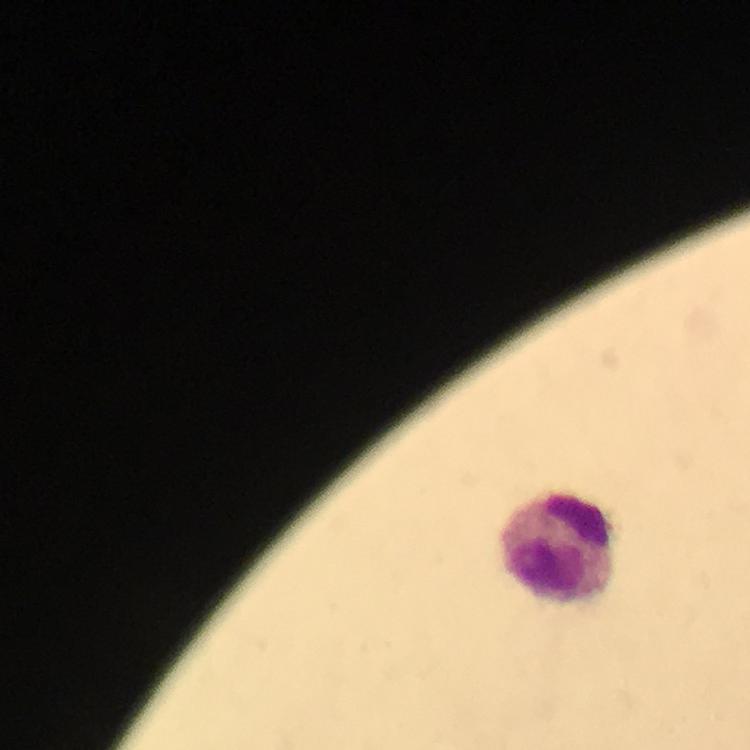

malaria parasites = none detected
context = from a diagnostic examination for malaria
magnification = 100x
stain = Giemsa
preparation = thick blood smear
image size = 750×750 pixels
cropped from = a single field of view
immersion oil = applied
capture = smartphone mounted on the microscope
leukocyte locations = approximate centers as [x, y] in pixels: [565, 554]